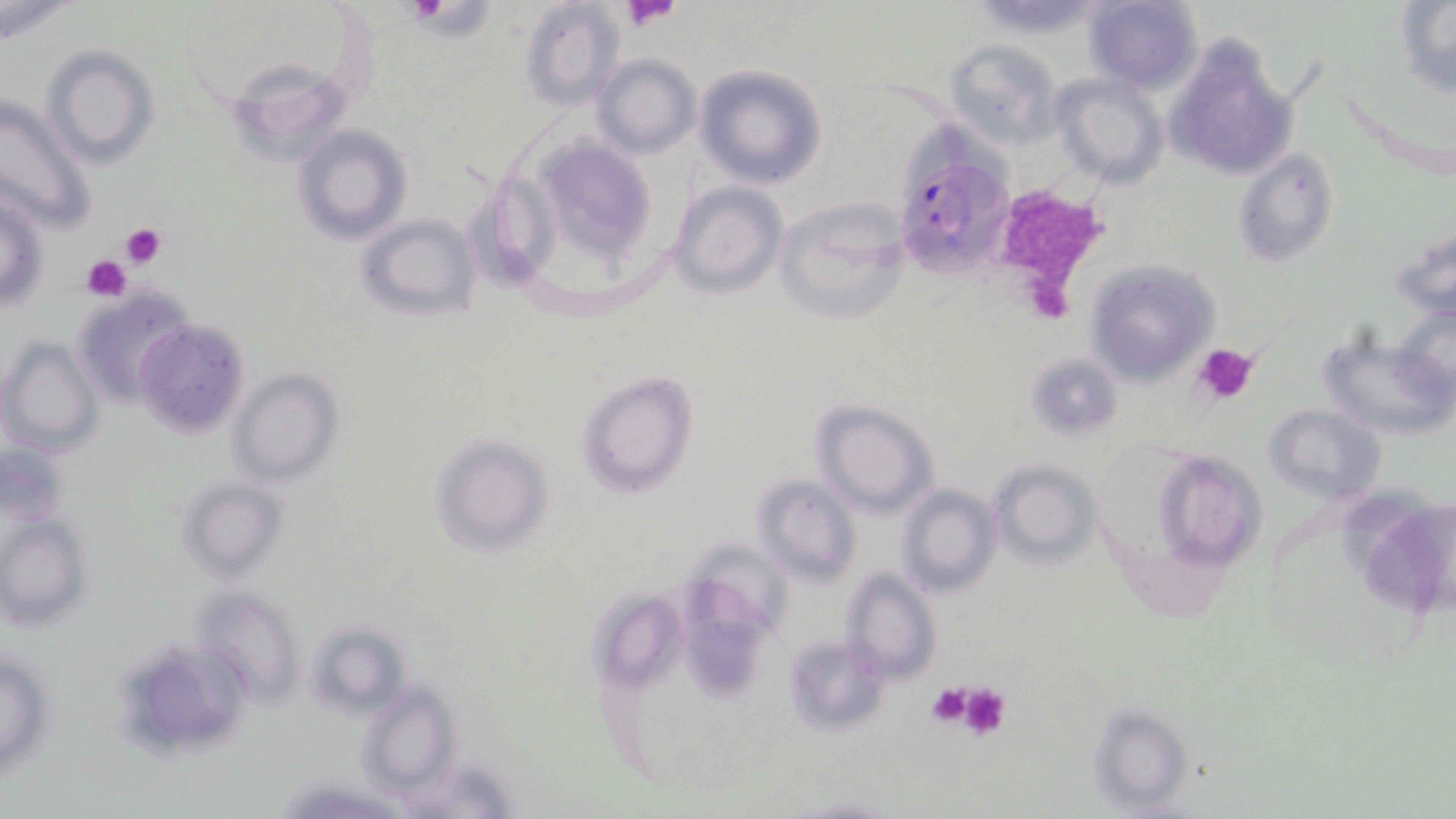

Approximate bounding boxes as [x1, y1, x2, y2] in pixels. Platelet locations: [619, 0, 682, 32], [411, 2, 490, 40], [1009, 188, 1097, 318], [119, 221, 167, 270], [82, 254, 131, 300], [1193, 342, 1259, 404], [924, 682, 975, 731], [957, 684, 1012, 742]. Uninfected red blood cell locations: [1081, 0, 1202, 93], [519, 1, 625, 113], [1395, 1, 1456, 99], [0, 2, 78, 44], [1162, 35, 1297, 185], [945, 38, 1062, 148], [39, 44, 160, 171], [590, 53, 701, 159], [694, 64, 828, 189], [227, 70, 343, 147], [1051, 74, 1168, 189], [0, 94, 96, 236], [292, 124, 412, 244], [515, 129, 659, 271], [1233, 146, 1337, 266], [471, 170, 566, 290], [668, 182, 788, 297], [0, 186, 48, 314], [773, 197, 914, 326], [357, 213, 481, 321], [1082, 259, 1218, 386], [71, 287, 193, 408], [1390, 303, 1455, 404], [134, 319, 250, 440], [1314, 328, 1456, 440], [0, 337, 102, 455], [1026, 351, 1124, 438], [227, 368, 343, 488], [577, 371, 698, 497], [812, 399, 938, 517], [1265, 403, 1388, 503], [430, 433, 552, 557], [4, 442, 69, 527], [1155, 451, 1263, 572], [988, 460, 1102, 570], [753, 474, 861, 585], [178, 478, 288, 582], [895, 483, 1001, 598], [1350, 499, 1456, 627], [0, 512, 92, 631], [688, 539, 802, 639], [841, 567, 942, 685], [682, 582, 774, 706], [186, 584, 305, 709], [593, 587, 689, 688], [306, 619, 412, 718], [782, 633, 889, 736], [0, 650, 57, 778], [358, 679, 460, 797], [1086, 701, 1195, 814], [792, 792, 900, 817]. Plasmodium falciparum-infected red blood cell locations: [897, 163, 1015, 276]. Slide-level diagnosis: Plasmodium falciparum. One field of a larger specimen. Image is 1456×819 pixels. May-Grünwald-Giemsa stain. 1000x magnification. Light microscopy. Thin blood film.